Locate every Plasmodium parasite.
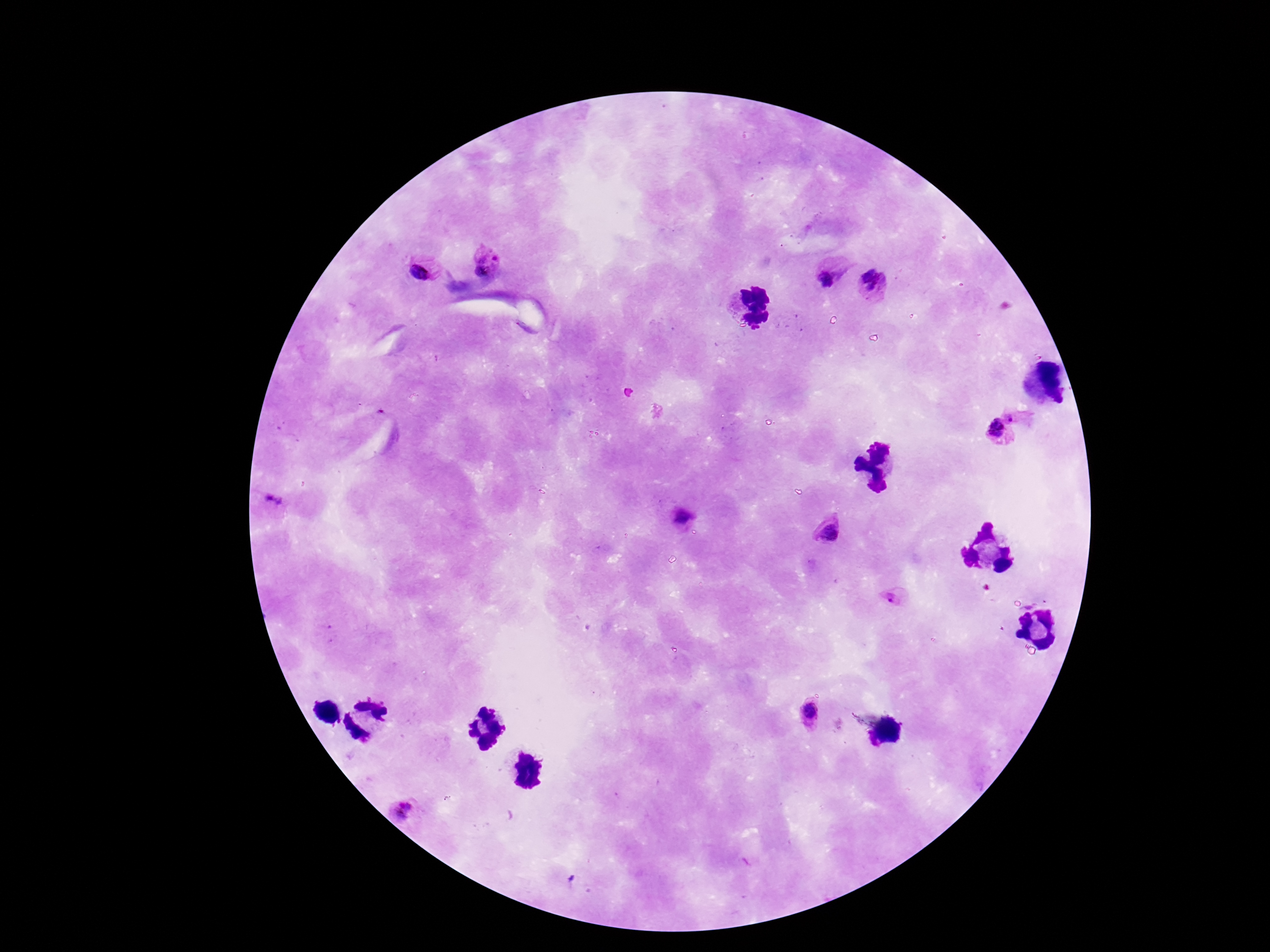
Approximate centers as (x, y) in pixels.
Plasmodium parasites: (496, 257), (480, 267), (420, 268), (829, 277), (876, 283), (1015, 417), (995, 432), (272, 501), (683, 518), (830, 530), (895, 595), (807, 711), (402, 808).

Summary:
  - Stain: Giemsa
  - Capture: smartphone camera through the microscope eyepiece
  - Patient malaria status: infected
  - Field of view: one from this slide
  - Magnification: 100x
  - Preparation: thick blood film
  - Image size: 1270×952 pixels